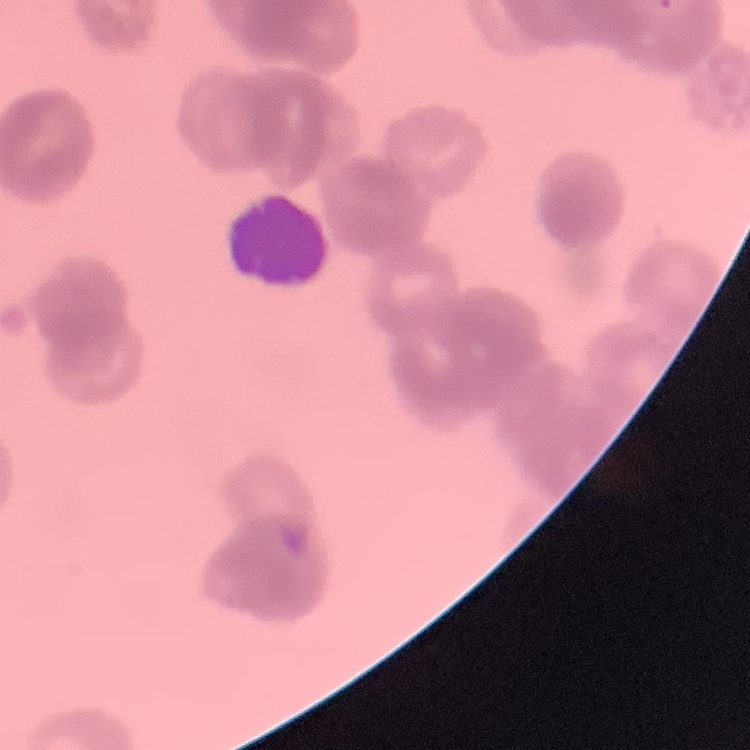
The erythrocytes show rouleaux formation. Thin blood film. Stained with either Field's or Giemsa. One tile cut from a larger photomicrograph.